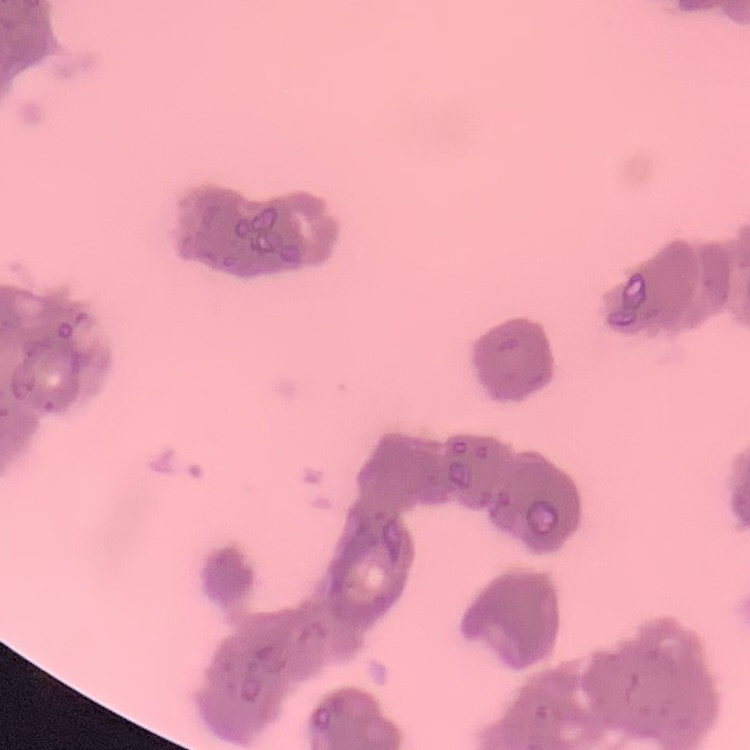

The red blood cells show rouleaux formation. Field's or Giemsa stain. Square crop of a larger photomicrograph. Thin peripheral smear.